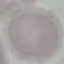 Result: no malaria parasites seen. Automatically extracted cell patch, resized to 64 × 64 pixels. Thin smear of blood. Acquired by smartphone through the microscope eyepiece. Giemsa stain.